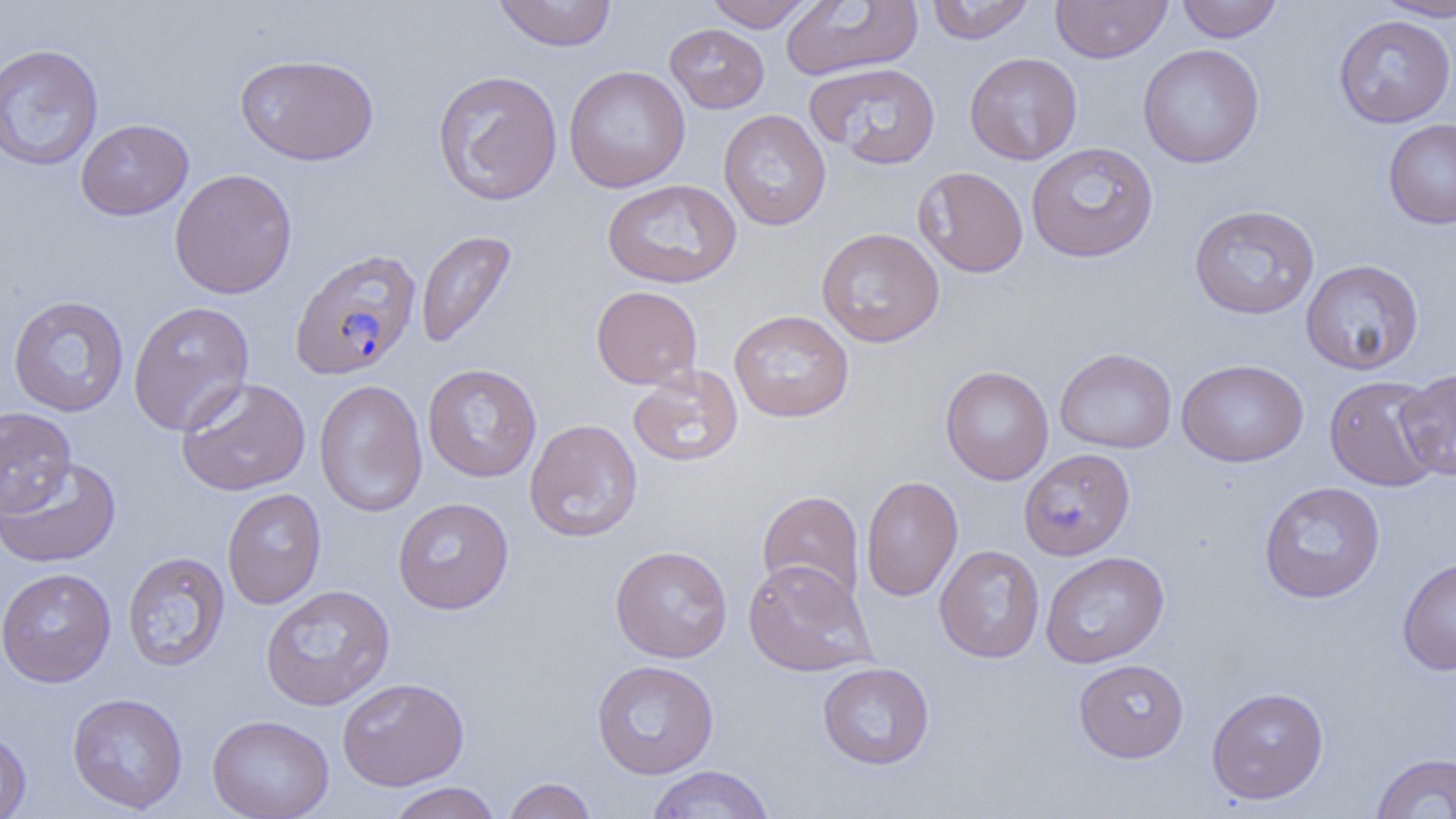

{
  "slide_level_diagnosis": "Plasmodium falciparum",
  "field_of_view": "one of a larger specimen",
  "plasmodium_falciparum_infected_red_blood_cell_locations": "approximate bounding boxes as (x1,y1)-(x2,y2) corner pairs in pixels: (289,248)-(422,381)",
  "image_size": "1456×819 pixels",
  "uninfected_red_blood_cell_locations": "approximate bounding boxes as (x1,y1)-(x2,y2) corner pairs in pixels: (492,0)-(617,51), (781,0)-(923,81), (926,0)-(1036,44), (1051,0)-(1172,63), (1176,0)-(1283,43), (1373,0)-(1456,20), (705,1)-(817,31), (1333,15)-(1455,128), (665,23)-(769,113), (0,43)-(104,172), (1138,44)-(1265,168), (965,52)-(1083,165), (235,53)-(379,166), (805,61)-(942,168), (563,65)-(690,192), (432,69)-(563,206), (718,109)-(832,231), (76,118)-(194,220), (1383,119)-(1456,229), (1026,141)-(1158,263), (913,166)-(1028,278), (169,168)-(298,298), (602,178)-(741,288), (1188,204)-(1321,320), (816,227)-(945,347), (416,230)-(518,350), (1300,259)-(1424,375), (590,285)-(703,390), (8,295)-(129,417), (128,300)-(254,436), (729,310)-(854,423), (1054,347)-(1177,453), (1176,358)-(1309,467), (422,363)-(542,482), (627,365)-(744,468), (940,365)-(1054,485), (1395,369)-(1456,480), (1324,375)-(1443,491), (175,377)-(311,496), (314,379)-(428,517), (0,406)-(77,515), (525,419)-(643,543), (1019,447)-(1135,560), (0,457)-(121,568), (861,475)-(963,601), (1259,481)-(1385,604), (222,487)-(326,609), (757,490)-(865,605), (393,497)-(514,614), (935,544)-(1045,663), (610,545)-(733,662), (122,551)-(230,672), (1041,551)-(1169,668), (1397,555)-(1456,676), (742,559)-(876,677), (0,567)-(117,687), (260,585)-(395,710), (1074,659)-(1189,762), (591,660)-(719,779), (818,662)-(934,769), (337,677)-(469,790), (1206,686)-(1329,804), (67,693)-(188,814), (207,714)-(334,819), (0,727)-(31,819), (1370,752)-(1456,818), (646,765)-(775,818), (502,777)-(597,819), (387,782)-(502,819)",
  "preparation": "thin blood film",
  "modality": "light microscopy",
  "magnification": "1000x"
}